Report the malaria status of this cell.
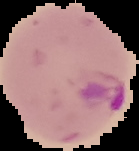

It is parasitized.

Summary:
  - Image type: segmented cell region on a black background
  - Preparation: thin blood smear
  - Image size: 139×151 pixels